Point out each Plasmodium parasite.
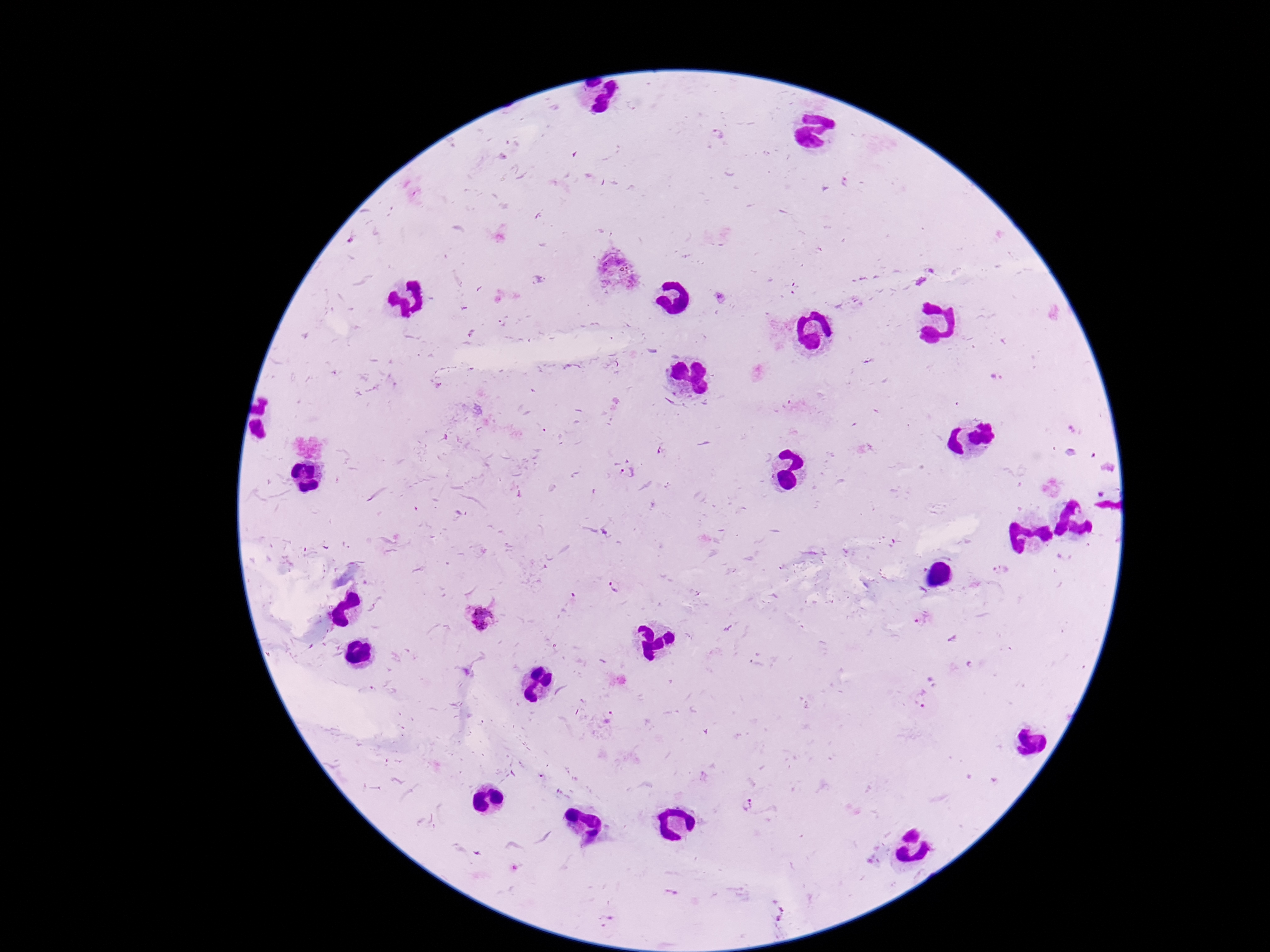

Approximate centers as {x, y} in pixels.
Plasmodium parasites: {717, 133}, {847, 183}, {540, 280}, {720, 296}, {663, 452}, {629, 474}, {999, 569}, {612, 586}, {480, 617}, {923, 619}, {921, 700}, {747, 806}, {672, 893}.

Patient malaria status: infected. Smartphone photograph taken through the microscope eyepiece. 100x magnification. Image is 1270×952 pixels. One field from this slide. Giemsa-stained preparation. Thick blood smear.